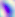 Micrograph. Toxoplasma gondii is seen. Captured at 400x magnification.